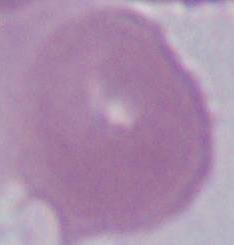
1000x magnification. Micrograph. An erythrocyte is seen.